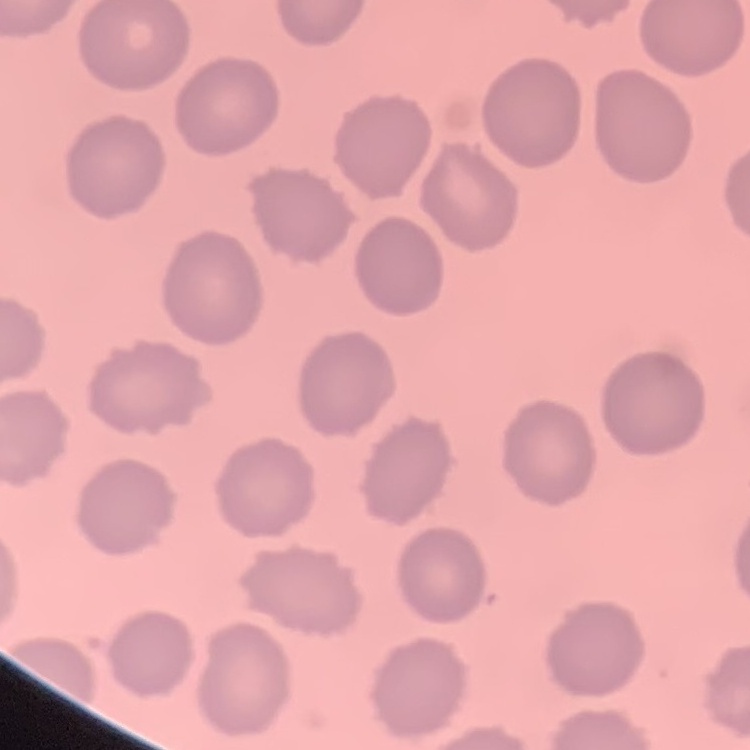
The erythrocytes exhibit no rouleaux formation. Thin blood film. Stained with either Field's or Giemsa. Square crop of a larger photomicrograph.